Outline each Plasmodium ovale-infected red blood cell.
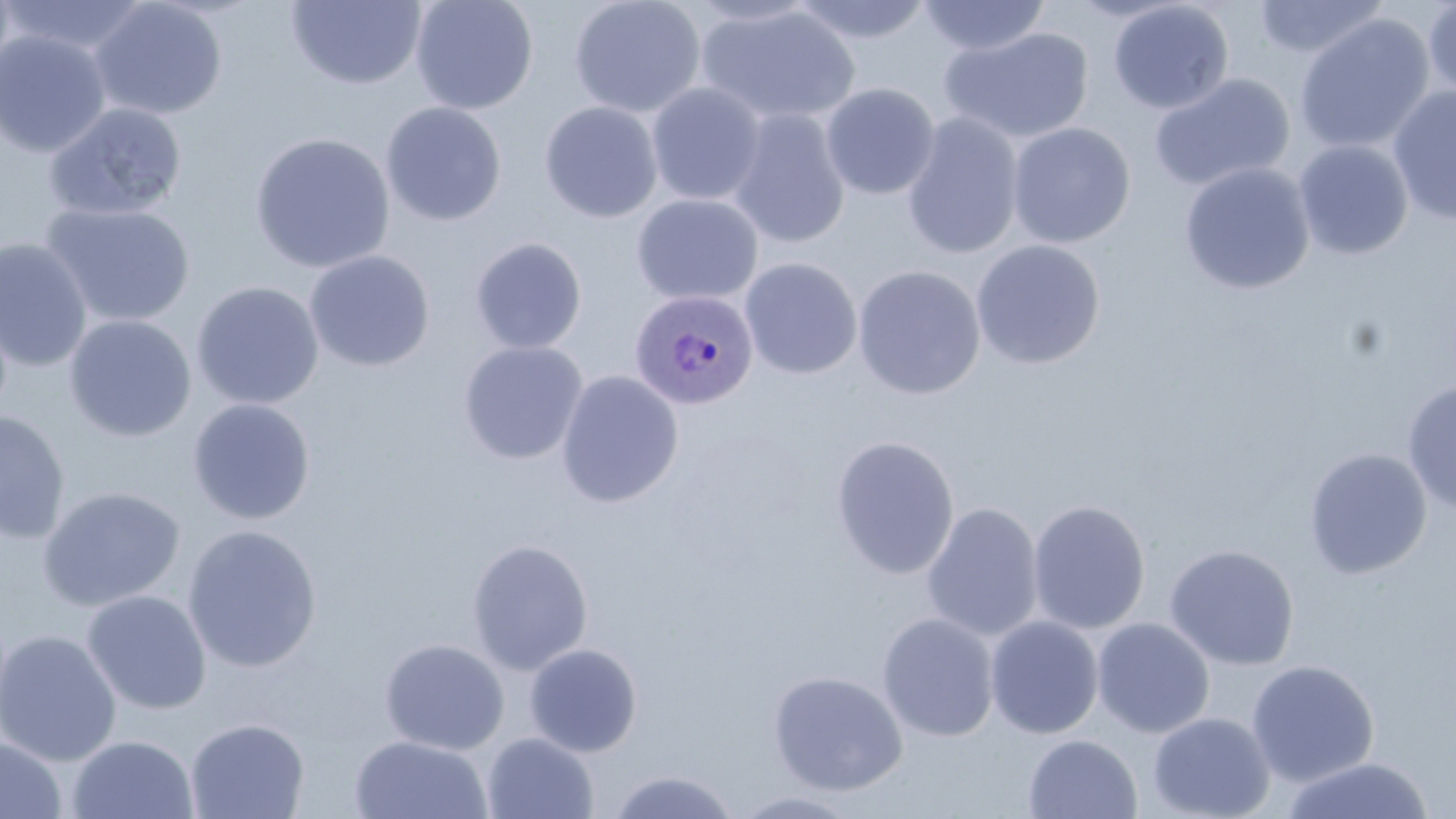
Approximate bounding boxes as (x1, y1, x2, y2) in pixels.
Plasmodium ovale-infected red blood cells: (629, 289, 759, 411).

Uninfected red blood cell locations: (0, 0, 153, 60), (286, 0, 428, 90), (410, 0, 539, 115), (568, 0, 706, 118), (788, 0, 936, 44), (1253, 0, 1390, 60), (1421, 0, 1456, 103), (91, 1, 228, 120), (916, 1, 1052, 57), (1107, 1, 1234, 114), (696, 5, 860, 127), (1293, 12, 1435, 155), (940, 26, 1094, 143), (0, 30, 112, 158), (1148, 73, 1294, 192), (646, 82, 767, 207), (820, 82, 941, 200), (1388, 85, 1456, 226), (539, 101, 663, 223), (43, 102, 188, 222), (380, 102, 507, 226), (727, 109, 851, 248), (901, 113, 1024, 260), (1007, 122, 1135, 248), (249, 132, 395, 274), (1293, 139, 1414, 260), (1179, 162, 1315, 295), (631, 194, 763, 306), (40, 202, 195, 328), (469, 237, 587, 354), (0, 238, 94, 372), (970, 239, 1106, 370), (304, 251, 435, 372), (740, 258, 862, 380), (852, 265, 986, 400), (191, 281, 324, 410), (63, 315, 196, 442), (458, 341, 588, 465), (555, 370, 684, 508), (1402, 379, 1456, 515), (186, 398, 316, 524), (0, 410, 71, 544), (830, 435, 960, 579), (1303, 448, 1432, 580), (37, 486, 186, 612), (1027, 499, 1151, 635), (920, 502, 1044, 642), (183, 524, 322, 673), (465, 538, 594, 675), (1164, 544, 1300, 670), (81, 589, 212, 715), (877, 612, 1000, 742), (984, 615, 1103, 739), (1092, 617, 1215, 738), (0, 629, 121, 766), (379, 638, 509, 755), (524, 642, 643, 757), (1246, 659, 1379, 786), (768, 670, 908, 796), (1147, 711, 1276, 819), (185, 717, 309, 819), (482, 731, 598, 819), (0, 734, 67, 819), (67, 734, 199, 819), (349, 734, 493, 819), (1023, 734, 1142, 819), (1279, 756, 1435, 819), (607, 769, 741, 819), (730, 790, 864, 818). Slide-level diagnosis: Plasmodium ovale. 1000x magnification. Thin blood smear. Light microscopy. One field of a larger specimen. Image is 1456×819 pixels. May-Grünwald-Giemsa-stained preparation.